Outline each Plasmodium falciparum parasite and classify it by life-cycle stage.
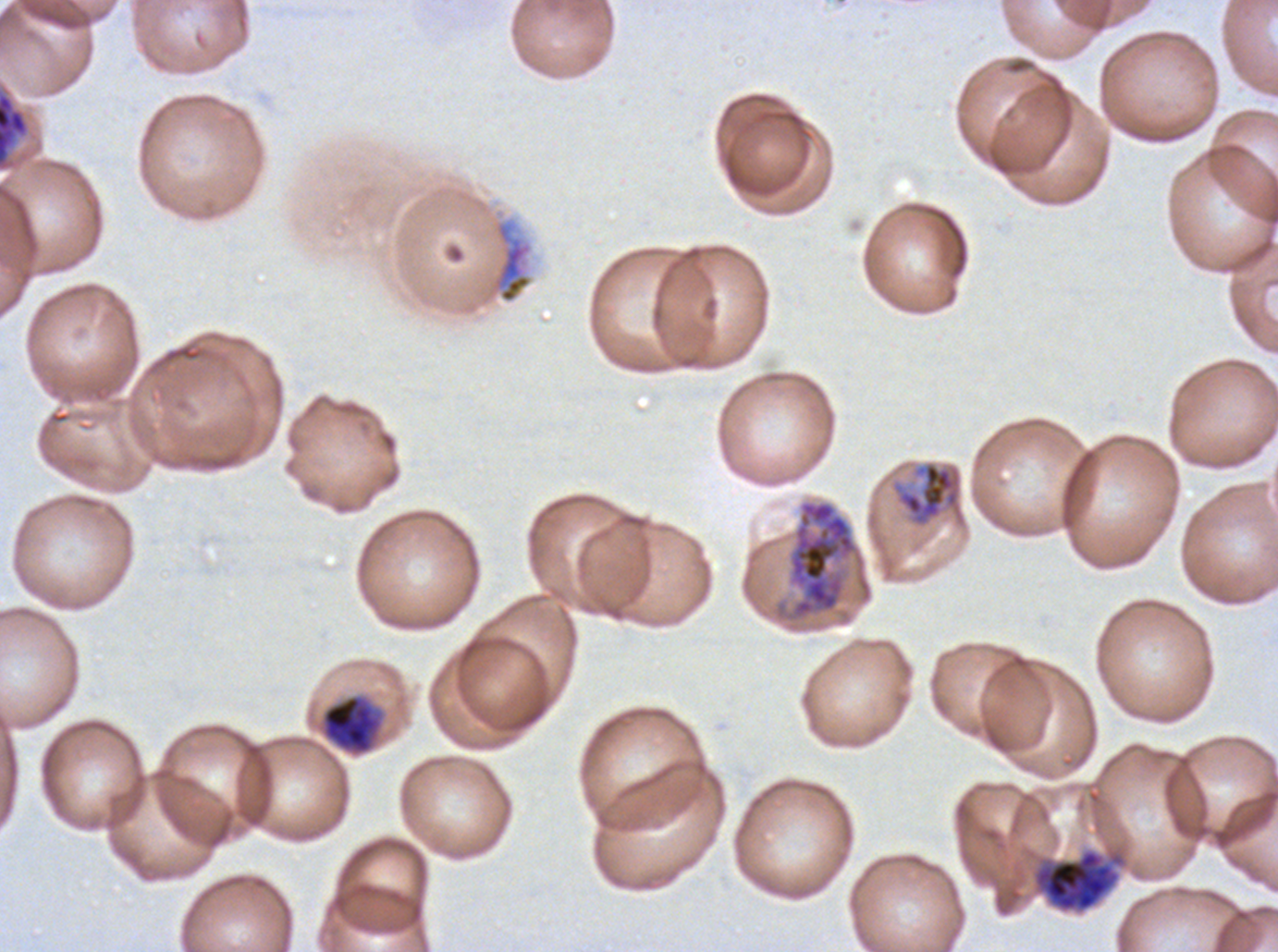
Approximate bounding rectangles given as corner coordinates in pixels from the top-left.
Mid trophozoites: (x1=897, y1=461, x2=962, y2=526).
Late trophozoites: (x1=321, y1=694, x2=383, y2=755).
Early schizonts: (x1=787, y1=499, x2=858, y2=621), (x1=1032, y1=848, x2=1124, y2=912).
No rings, late-ring/early-trophozoite forms, late schizonts, segmenters, or gametocytes observed.

Summary:
  - Debris locations: (x1=0, y1=92, x2=29, y2=166)
  - Preparation: thin blood film
  - Image size: 1278×952 pixels
  - Field of view: sub-image separated from a larger composite
  - Specimen: Plasmodium falciparum from a patient in The Gambia, cultured ex vivo for 24 to 48 hours
  - Life-cycle stages observed: mid trophozoite, late trophozoite, early schizont
  - Stain: Giemsa